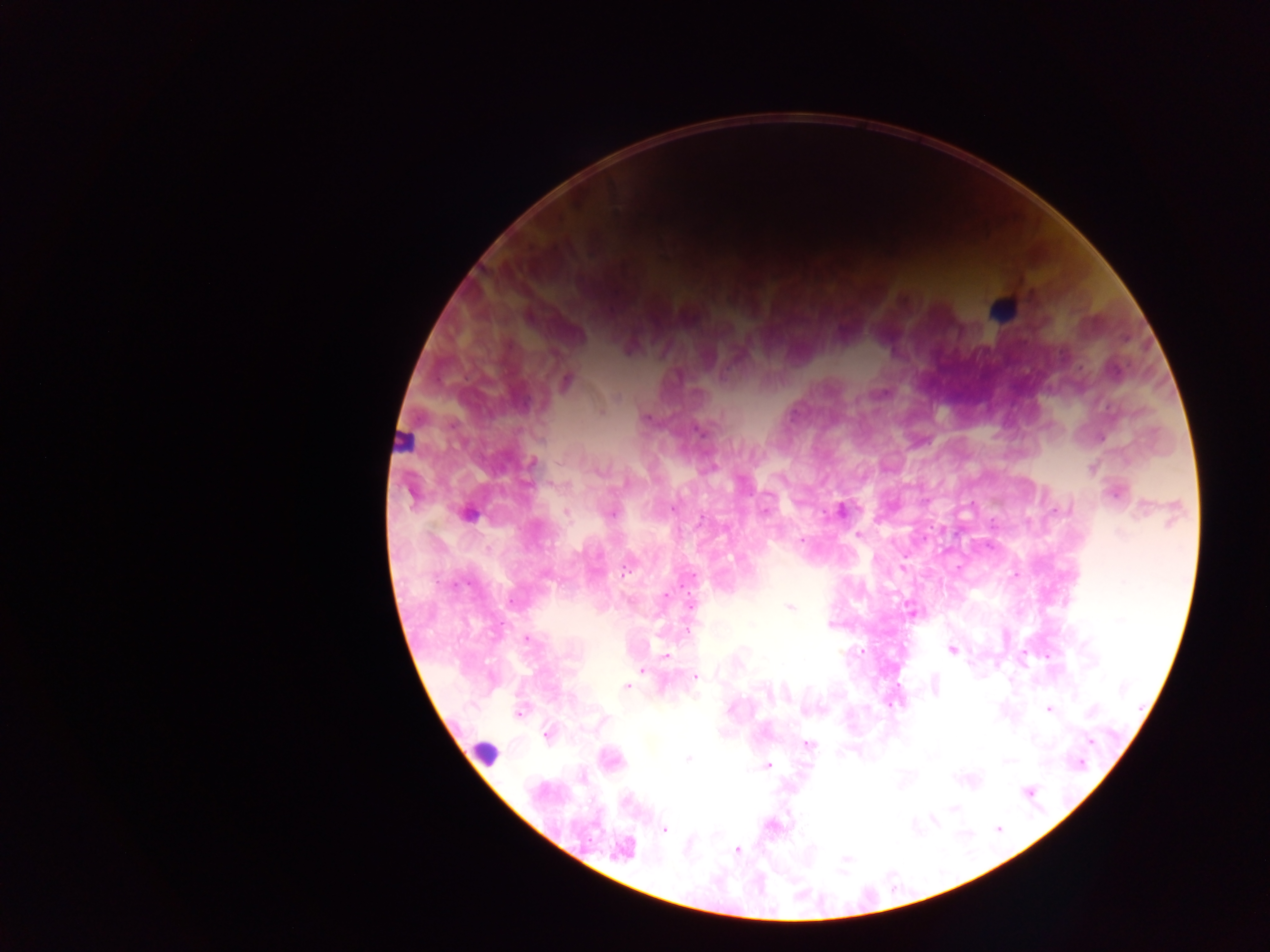 Approximate centers as [x, y] in pixels. Plasmodium parasite locations: [566, 382], [882, 393], [616, 397], [601, 411], [647, 419], [699, 431], [1102, 437], [532, 463], [1091, 469], [599, 472], [1114, 495], [411, 496], [673, 508], [1056, 509], [840, 511], [1141, 511], [611, 514], [701, 518], [857, 534], [1120, 534], [801, 540], [625, 572], [547, 577], [666, 595], [690, 604], [789, 607], [912, 612], [527, 639], [951, 650], [666, 657], [641, 670], [696, 677], [935, 686], [627, 687], [1049, 709], [1091, 711], [518, 713], [546, 735], [1089, 741], [808, 744], [689, 759], [1008, 761], [1080, 764], [768, 766], [1028, 791], [954, 808], [933, 820], [998, 829], [664, 830], [624, 848], [737, 850], [847, 858]. Leukocyte locations (subset; some below the resolvable size): [1002, 309], [400, 439], [469, 513], [484, 754]. Image is 1270×952 pixels. Thick blood film. Photographed through a microscope with a mobile-phone camera. One field of view. Collected in Ghana.